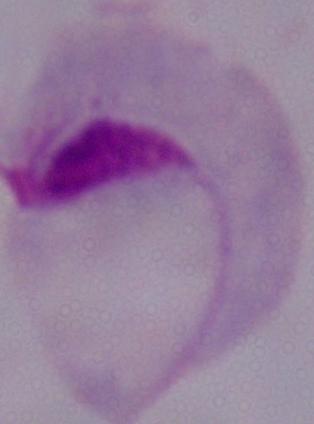

Summary:
  - Modality: photomicrograph
  - Identification: trichomonad
  - Magnification: 1000x